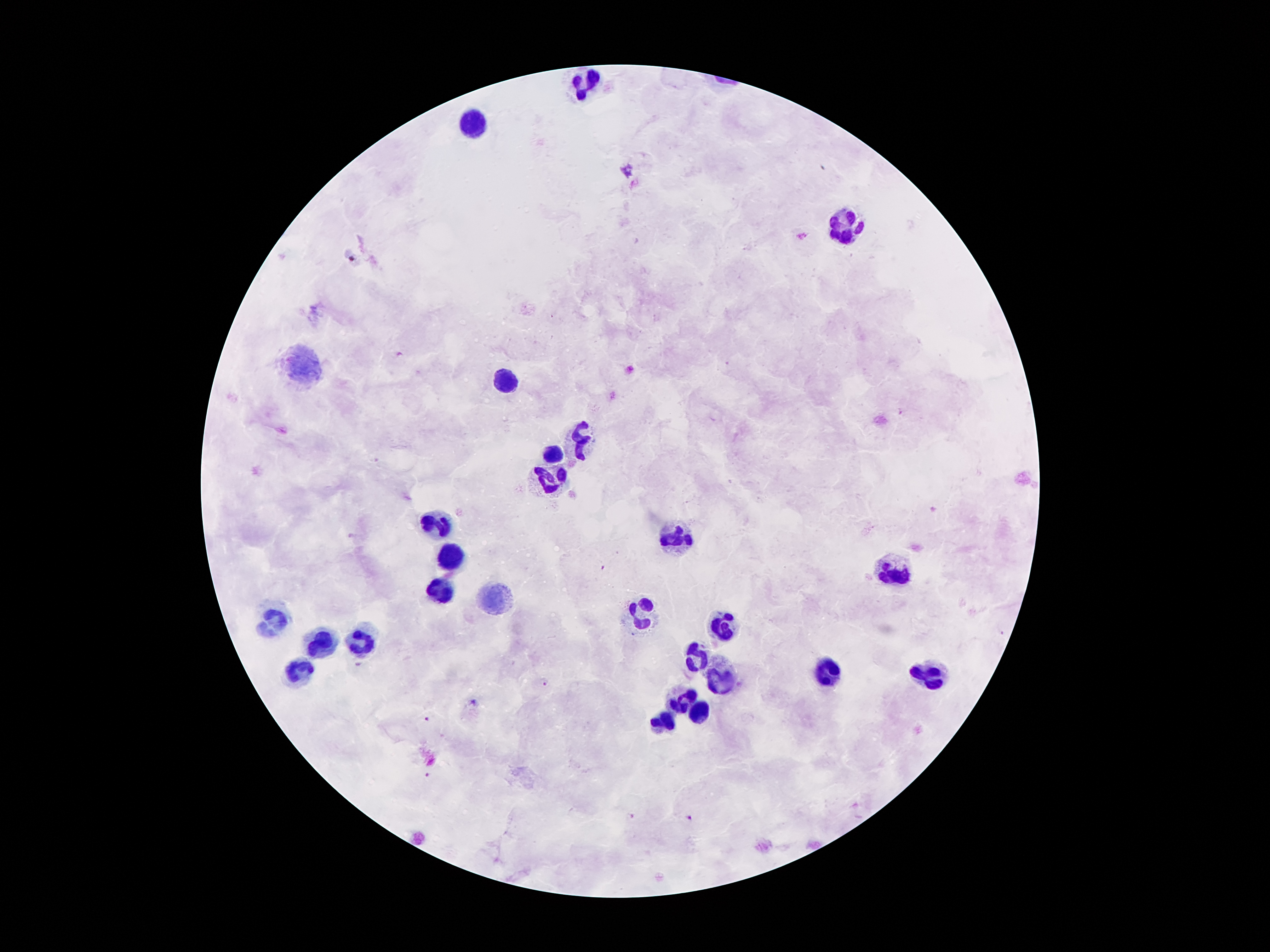

coordinate format = approximate centers as (x, y) in pixels
malaria parasite locations = (352, 259), (900, 411), (358, 663), (546, 682), (473, 702), (425, 719), (426, 776), (631, 816), (688, 818)
leukocyte locations = (590, 83), (470, 122), (848, 226), (296, 368), (500, 379), (584, 437), (552, 453), (552, 480), (437, 522), (676, 533), (453, 556), (890, 570), (439, 587), (497, 595), (644, 608), (269, 621), (724, 625), (357, 642), (321, 643), (699, 656), (827, 671), (300, 673), (934, 676), (722, 681), (682, 700), (701, 713), (665, 719)
patient malaria status = positive for Plasmodium falciparum
field of view = single
preparation = thick blood smear
capture = smartphone through the microscope eyepiece
magnification = 100x
image size = 1270×952 pixels
stain = Giemsa